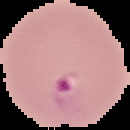

Summary:
  - Image size: 130×130 pixels
  - Preparation: thin blood film
  - Result: Plasmodium parasites detected
  - Image type: cell region segmented out of the field of view; surrounding area masked to black